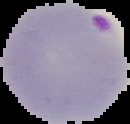
Summary:
  - Image type: segmented cell region on a black background
  - Image size: 130×124 pixels
  - Result: malaria parasites detected
  - Preparation: thin blood film